Assess the morphology of the red blood cells.
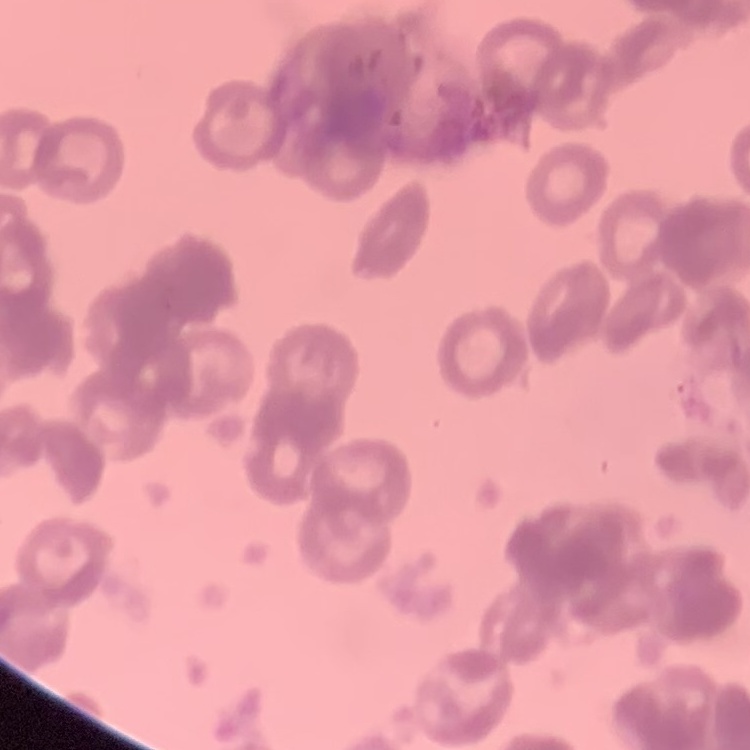
Rouleaux formation.

preparation = thin blood film
stain = Field's or Giemsa
image type = one tile cut from a larger photomicrograph